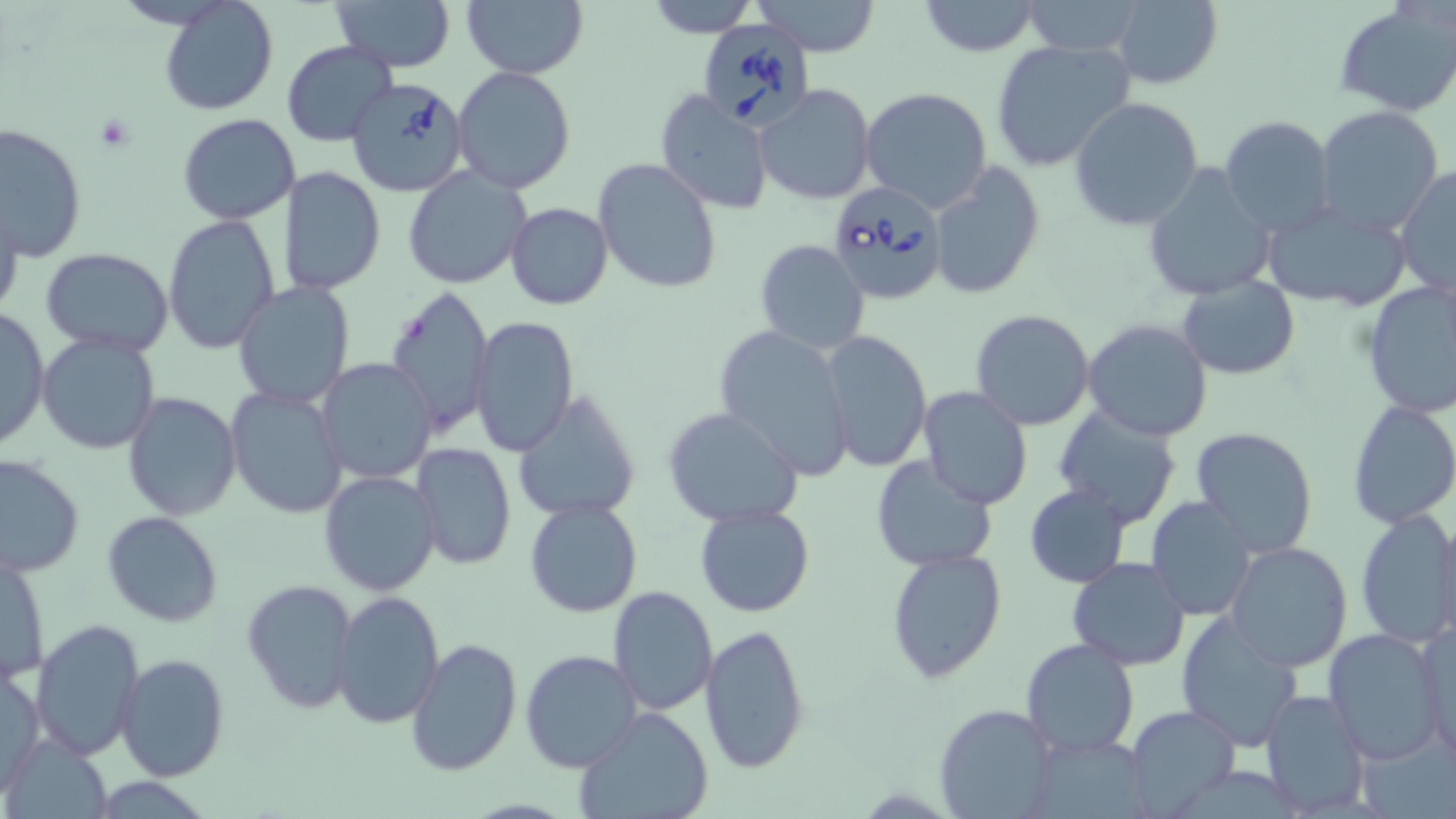
Approximate bounding boxes as (x1,y1)-(x2,y2) corner pairs in pixels. Uninfected red blood cell locations: (160,0)-(277,115), (332,0)-(456,72), (461,0)-(588,80), (647,0)-(760,38), (753,0)-(880,56), (1019,0)-(1148,57), (1112,0)-(1223,90), (917,1)-(1043,55), (1335,4)-(1456,115), (989,38)-(1135,172), (281,40)-(397,147), (451,66)-(577,195), (756,83)-(874,205), (861,87)-(993,213), (655,90)-(774,215), (1069,96)-(1204,230), (1312,107)-(1444,236), (177,113)-(301,224), (1218,116)-(1338,238), (1,123)-(87,262), (592,157)-(722,295), (929,164)-(1045,299), (1142,164)-(1276,300), (402,165)-(531,289), (278,167)-(386,296), (1393,167)-(1456,300), (0,193)-(23,325), (1260,199)-(1414,311), (506,202)-(613,310), (162,213)-(281,354), (754,239)-(871,354), (41,247)-(175,355), (1176,275)-(1300,380), (1360,280)-(1456,418), (231,281)-(354,410), (387,285)-(495,436), (0,307)-(50,453), (969,308)-(1095,430), (470,316)-(579,456), (1082,318)-(1215,441), (714,324)-(854,483), (822,329)-(933,474), (36,332)-(163,456), (315,357)-(439,484), (917,385)-(1034,511), (225,386)-(347,520), (512,389)-(642,524), (122,391)-(241,521), (1346,400)-(1456,530), (1052,406)-(1183,529), (662,407)-(803,528), (1189,426)-(1319,558), (410,442)-(516,570), (0,454)-(84,578), (870,456)-(998,573), (319,470)-(442,596), (1023,484)-(1131,587), (1145,496)-(1256,621), (524,499)-(643,618), (695,505)-(814,617), (1354,508)-(1456,648), (102,511)-(226,629), (1431,515)-(1455,645), (1223,540)-(1353,672), (886,547)-(1007,686), (1,549)-(50,686), (1067,559)-(1191,669), (242,578)-(360,713), (607,588)-(718,716), (331,590)-(444,729), (1173,611)-(1305,752), (30,617)-(144,762), (1414,617)-(1454,760), (699,623)-(811,772), (1323,629)-(1448,764), (1020,636)-(1141,757), (405,638)-(522,777), (519,650)-(641,774), (117,652)-(230,780), (1,665)-(45,797), (1260,689)-(1371,818), (934,703)-(1058,817), (1124,705)-(1241,817), (575,708)-(715,819), (1036,737)-(1157,819). Babesia divergens-infected red blood cell locations: (699,14)-(816,131), (344,74)-(470,197), (827,179)-(947,306). Platelet locations: (91,113)-(137,150). Slide-level diagnosis: Babesia divergens. One field of a larger specimen. Image is 1456×819 pixels. Captured at 1000x magnification. May-Grünwald-Giemsa-stained preparation. Thin blood smear. Light microscopy.